Outline each blood parasite and name the species.
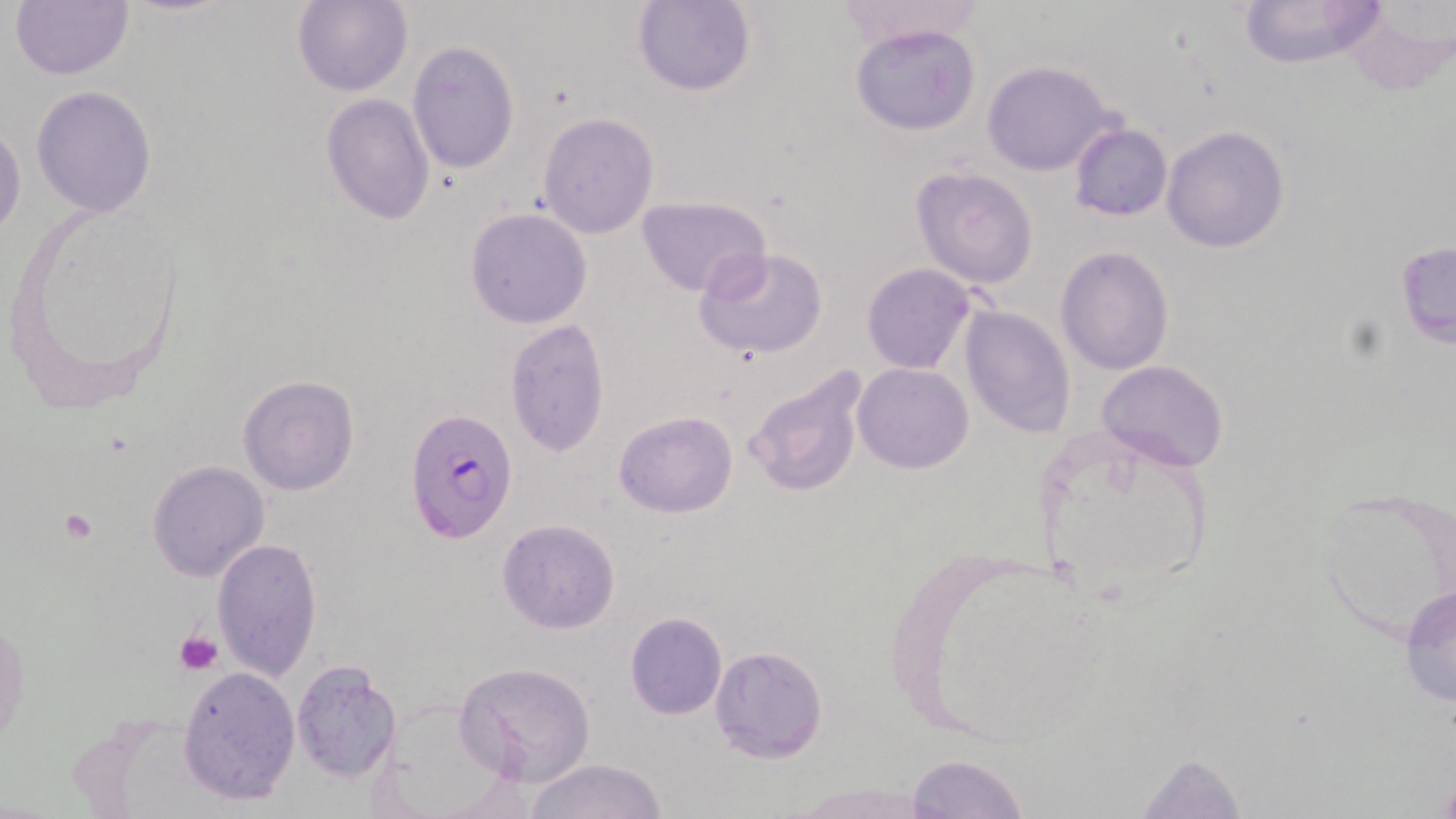
Approximate bounding boxes as named x1/y1/x2/y2 corners in pixels.
Plasmodium falciparum-infected red blood cells: (x1=407, y1=408, x2=518, y2=543).
No Plasmodium ovale, Plasmodium malariae, Plasmodium vivax, Babesia divergens, or Trypanosoma brucei observed.

{
  "slide_level_diagnosis": "Plasmodium falciparum",
  "stain": "May-Grünwald-Giemsa",
  "magnification": "1000x",
  "image_size": "1456×819 pixels",
  "field_of_view": "single",
  "platelet_locations": "approximate bounding boxes as named x1/y1/x2/y2 corners in pixels: (x1=58, y1=509, x2=99, y2=545), (x1=175, y1=632, x2=222, y2=674)",
  "preparation": "thin blood smear",
  "uninfected_red_blood_cell_locations": "approximate bounding boxes as named x1/y1/x2/y2 corners in pixels: (x1=11, y1=0, x2=133, y2=79), (x1=831, y1=0, x2=986, y2=51), (x1=1236, y1=0, x2=1389, y2=69), (x1=291, y1=1, x2=413, y2=97), (x1=632, y1=1, x2=755, y2=97), (x1=1341, y1=4, x2=1455, y2=96), (x1=850, y1=23, x2=982, y2=136), (x1=406, y1=41, x2=520, y2=176), (x1=982, y1=60, x2=1117, y2=177), (x1=31, y1=86, x2=157, y2=218), (x1=320, y1=94, x2=435, y2=224), (x1=537, y1=112, x2=659, y2=238), (x1=0, y1=122, x2=26, y2=241), (x1=1068, y1=123, x2=1174, y2=221), (x1=1161, y1=125, x2=1291, y2=254), (x1=909, y1=165, x2=1039, y2=288), (x1=636, y1=197, x2=771, y2=297), (x1=465, y1=208, x2=591, y2=328), (x1=1395, y1=242, x2=1455, y2=347), (x1=693, y1=246, x2=830, y2=360), (x1=1055, y1=246, x2=1174, y2=375), (x1=862, y1=263, x2=975, y2=374), (x1=958, y1=305, x2=1077, y2=440), (x1=505, y1=321, x2=611, y2=458), (x1=1097, y1=359, x2=1229, y2=474), (x1=853, y1=363, x2=973, y2=474), (x1=741, y1=365, x2=870, y2=500), (x1=238, y1=375, x2=360, y2=495), (x1=614, y1=411, x2=738, y2=518), (x1=1031, y1=420, x2=1220, y2=612), (x1=148, y1=461, x2=270, y2=583), (x1=1315, y1=488, x2=1456, y2=642), (x1=496, y1=519, x2=621, y2=635), (x1=210, y1=537, x2=322, y2=681), (x1=883, y1=538, x2=1115, y2=744), (x1=1398, y1=583, x2=1456, y2=713), (x1=625, y1=611, x2=726, y2=719), (x1=0, y1=612, x2=26, y2=754), (x1=709, y1=644, x2=828, y2=763), (x1=290, y1=659, x2=402, y2=783), (x1=453, y1=661, x2=595, y2=786), (x1=177, y1=666, x2=302, y2=805), (x1=1127, y1=749, x2=1251, y2=817), (x1=906, y1=753, x2=1030, y2=819), (x1=527, y1=758, x2=667, y2=819), (x1=793, y1=781, x2=930, y2=817)",
  "modality": "light microscopy"
}